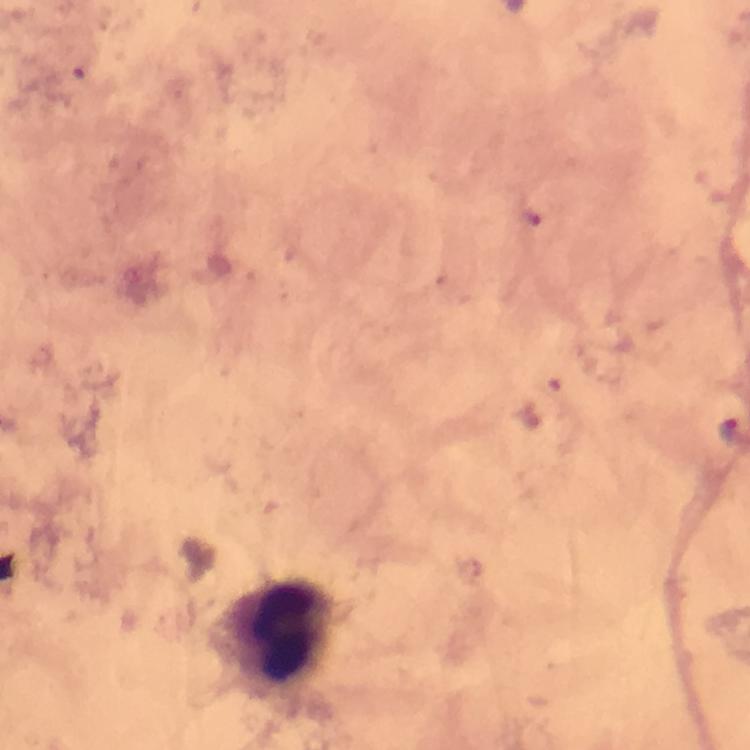

magnification: 100x
capture: smartphone mounted on the microscope
image_size: 750×750 pixels
preparation: thick smear
immersion_oil: used
context: from a diagnostic examination for malaria
stain: Giemsa
malaria_parasite_locations: 'approximate centers as [x, y] in pixels: [731, 433]'
leukocyte_locations: 'approximate centers as [x, y] in pixels: [278, 633]'
cropped_from: a single field of view